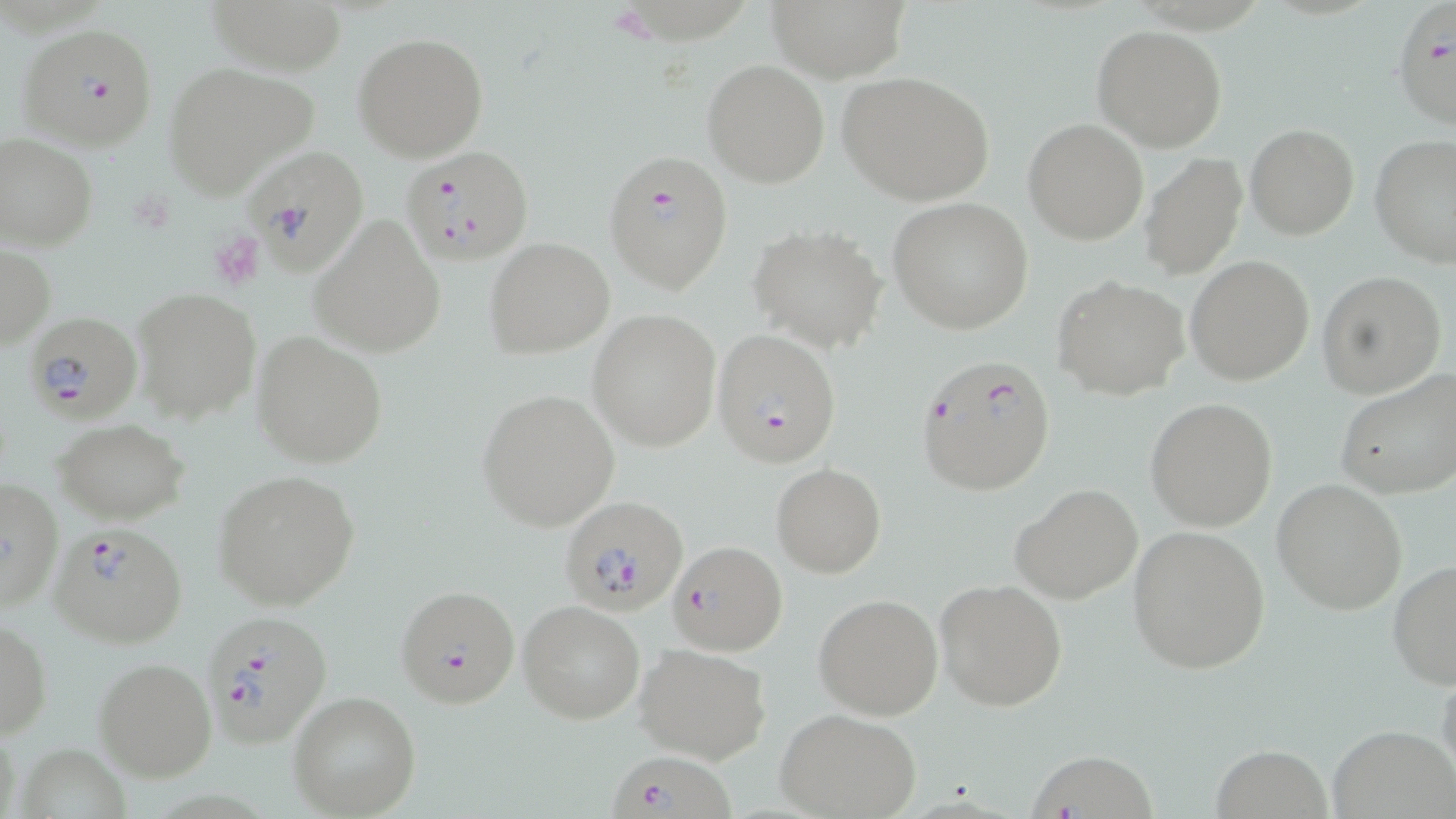
{
  "slide_level_diagnosis": "Plasmodium falciparum",
  "image_size": "1456×819 pixels",
  "plasmodium_falciparum_infected_red_blood_cell_locations": "approximate bounding boxes as [x1, y1, x2, y2] in pixels: [1392, 3, 1455, 130], [16, 20, 161, 151], [240, 143, 368, 276], [402, 145, 533, 267], [604, 149, 733, 294], [22, 311, 143, 424], [713, 329, 841, 467], [914, 354, 1056, 496], [564, 495, 690, 613], [48, 521, 188, 650], [671, 541, 786, 654], [396, 585, 520, 709], [199, 610, 333, 750], [1028, 747, 1164, 819], [608, 755, 732, 819]",
  "field_of_view": "single",
  "modality": "optical microscopy",
  "stain": "May-Grünwald-Giemsa",
  "preparation": "thin blood smear",
  "magnification": "1000x",
  "uninfected_red_blood_cell_locations": "approximate bounding boxes as [x1, y1, x2, y2] in pixels: [209, 0, 347, 76], [761, 0, 913, 82], [1092, 25, 1227, 153], [353, 32, 489, 162], [702, 59, 830, 187], [162, 62, 319, 197], [837, 71, 996, 205], [1023, 119, 1149, 244], [1245, 123, 1359, 240], [0, 133, 97, 251], [1371, 135, 1455, 267], [1141, 152, 1247, 278], [887, 199, 1034, 334], [309, 215, 447, 357], [752, 226, 889, 354], [485, 237, 615, 357], [1, 243, 53, 351], [1186, 256, 1314, 387], [1317, 270, 1445, 398], [1051, 274, 1190, 400], [131, 289, 261, 422], [589, 310, 721, 450], [252, 332, 388, 469], [1335, 368, 1456, 501], [476, 389, 621, 530], [1146, 399, 1278, 533], [54, 419, 190, 524], [771, 463, 887, 578], [212, 470, 360, 610], [1, 477, 64, 613], [1272, 479, 1407, 613], [1012, 484, 1143, 603], [1128, 524, 1270, 674], [1388, 559, 1456, 690], [935, 579, 1068, 712], [814, 595, 943, 720], [517, 599, 645, 724], [1, 617, 51, 740], [633, 642, 771, 765], [94, 657, 216, 781], [1436, 659, 1456, 792], [287, 691, 421, 818], [775, 708, 922, 819], [1328, 725, 1456, 819], [1211, 744, 1333, 817]"
}